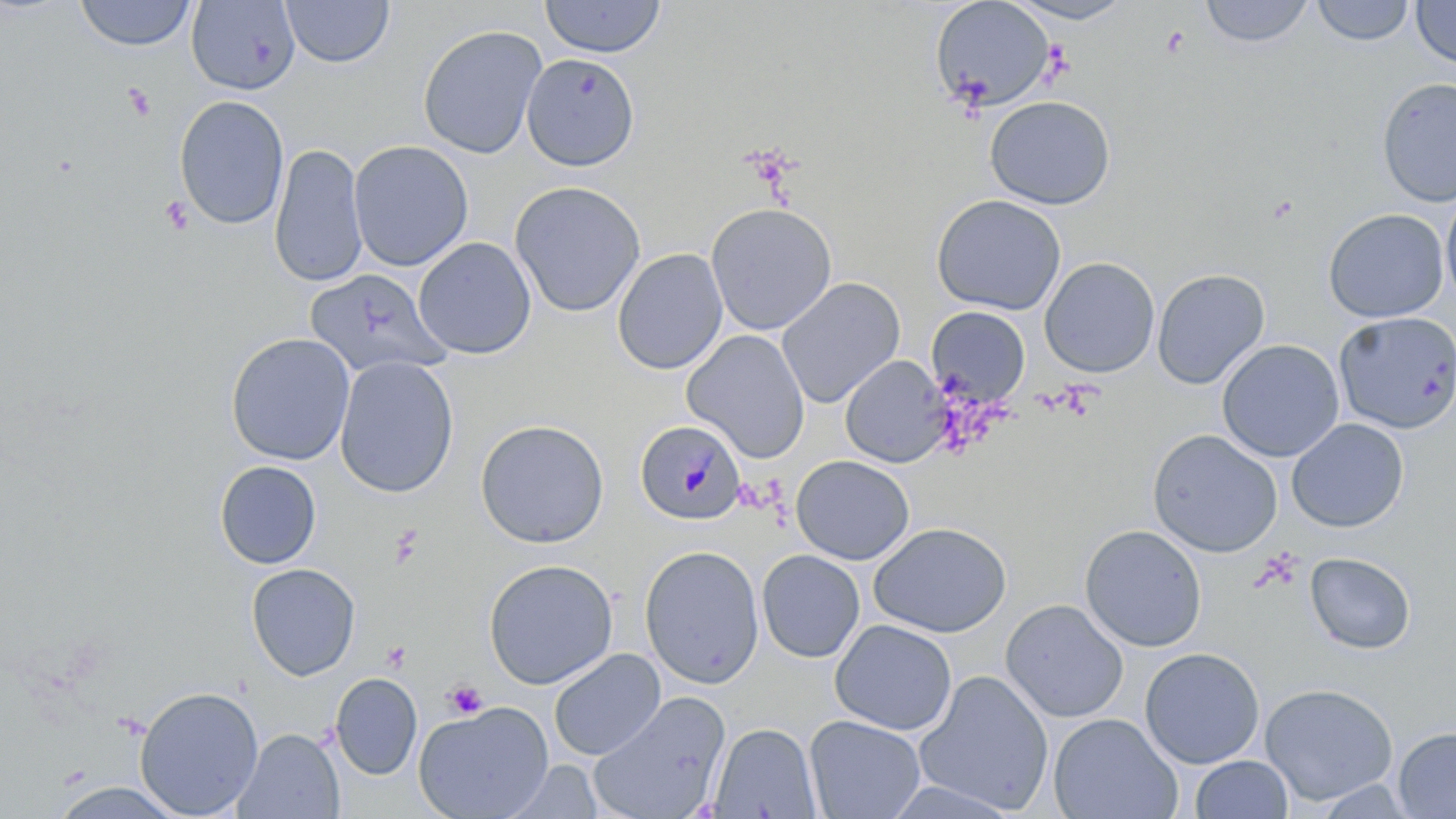

Approximate bounding boxes as (x1, y1, x2, y2) in pixels. Platelet locations: (122, 82, 155, 121), (161, 196, 194, 235), (389, 527, 423, 569), (443, 679, 488, 720). Uninfected red blood cell locations: (281, 0, 394, 68), (539, 0, 667, 58), (929, 0, 1057, 113), (1002, 0, 1140, 25), (1200, 0, 1314, 48), (1311, 0, 1415, 46), (74, 1, 196, 51), (186, 1, 301, 95), (1411, 1, 1456, 69), (417, 24, 547, 159), (521, 53, 640, 172), (1376, 76, 1456, 207), (174, 95, 290, 229), (984, 95, 1116, 210), (349, 140, 473, 271), (269, 143, 368, 288), (509, 180, 646, 318), (1440, 190, 1456, 312), (930, 194, 1067, 316), (705, 202, 838, 336), (1323, 208, 1449, 323), (413, 237, 536, 360), (612, 247, 728, 375), (1039, 257, 1160, 378), (306, 268, 449, 379), (1151, 268, 1270, 389), (776, 277, 905, 408), (926, 306, 1030, 406), (1333, 311, 1456, 433), (682, 330, 810, 462), (225, 332, 355, 466), (1217, 339, 1345, 462), (840, 355, 950, 468), (335, 356, 458, 498), (1287, 418, 1409, 533), (474, 419, 610, 548), (1147, 428, 1283, 558), (791, 455, 915, 565), (215, 460, 322, 569), (869, 522, 1012, 638), (1079, 524, 1207, 652), (639, 544, 765, 689), (756, 549, 866, 663), (1304, 552, 1416, 654), (483, 558, 618, 689), (245, 563, 361, 681), (1000, 599, 1128, 723), (830, 619, 957, 736), (1139, 647, 1265, 769), (548, 648, 666, 761), (914, 670, 1053, 814), (330, 672, 422, 781), (1259, 683, 1399, 806), (134, 685, 264, 818), (587, 691, 730, 819), (413, 700, 554, 819), (1049, 713, 1181, 819), (804, 714, 926, 819), (709, 722, 822, 818), (1393, 726, 1456, 818), (234, 728, 344, 818), (1190, 755, 1294, 818), (502, 760, 603, 818), (881, 780, 1025, 819), (50, 781, 189, 818). Plasmodium malariae-infected red blood cell locations: (635, 419, 747, 525). Slide-level diagnosis: Plasmodium malariae. One field of a larger specimen. Thin blood film. Captured at 1000x magnification. Optical microscopy. May-Grünwald-Giemsa stain. Image is 1456×819 pixels.